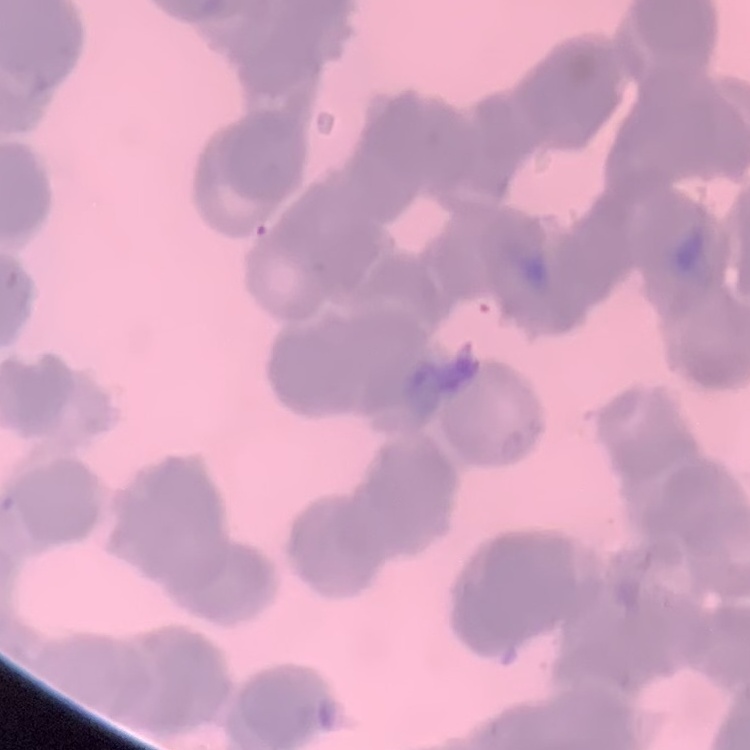 The red blood cells exhibit rouleaux formation. Thin blood film. Stained with either Field's or Giemsa. One tile cut from a larger photomicrograph.